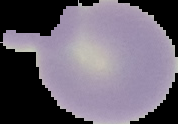
From a thin blood smear. Image is 178×124 pixels. Segmented cell region on a black background. Malaria status: uninfected.